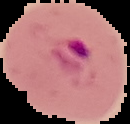
Summary:
  - Result: Plasmodium parasites detected
  - Preparation: thin blood film
  - Image size: 130×124 pixels
  - Image type: segmented cell region with the area outside set to black